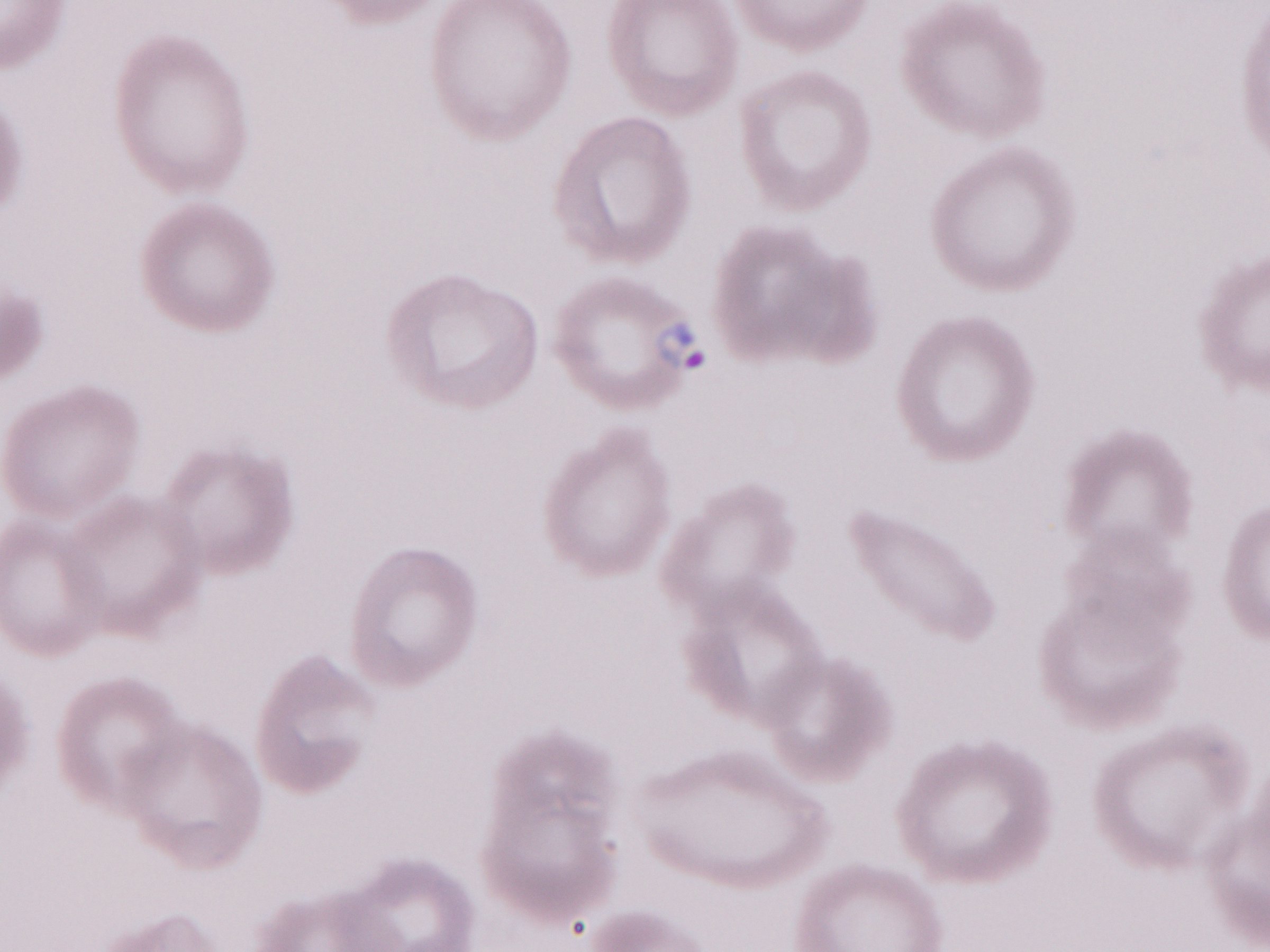

Magnification: 1,000x. One field of this slide. Olympus BX43 microscope and DP73 digital camera. Patient-level malaria diagnosis: positive. Thin peripheral-blood smear. May-Grünwald-Giemsa stain. Image is 1270×952 pixels.